Report the malaria status of this cell.
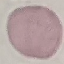
It is uninfected.

{
  "stain": "Giemsa",
  "image_type": "automatically extracted cell patch, resized to 64 × 64 pixels",
  "capture": "smartphone camera at the microscope eyepiece",
  "preparation": "thin blood film"
}